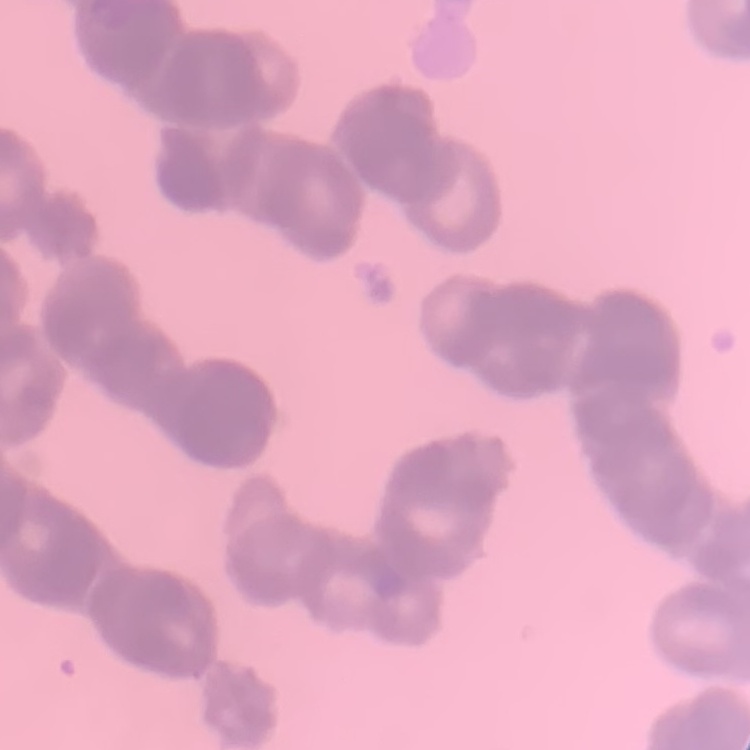

Summary:
  - Erythrocyte morphology: rouleaux formation
  - Preparation: thin blood film
  - Image type: one tile cut from a larger photomicrograph
  - Stain: Field's or Giemsa